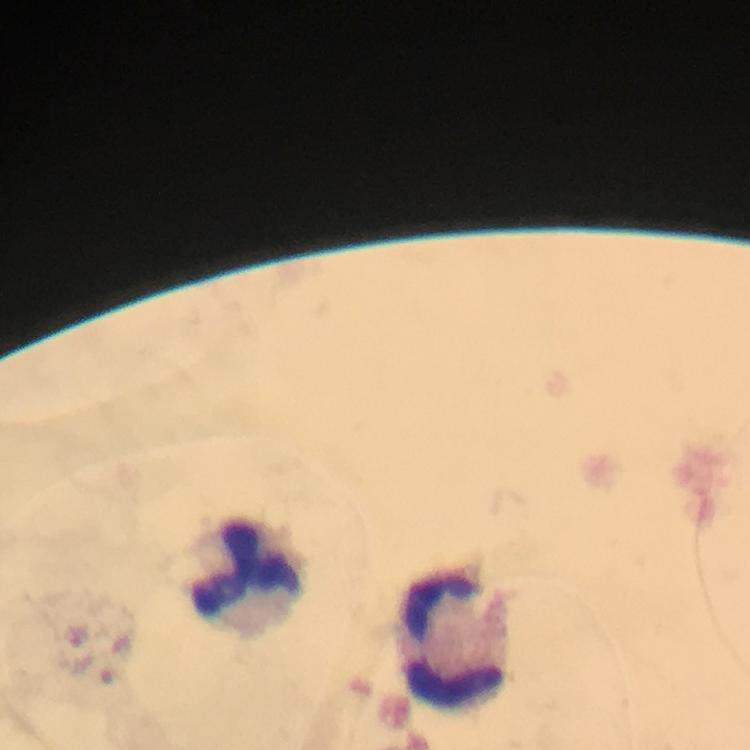
Approximate centers as (x, y) in pixels. Leukocyte locations: (248, 572), (456, 638). Image is 750×750 pixels. Giemsa-stained preparation. Immersion oil was used. Malaria parasites: none seen. Photographed with a smartphone mounted on the microscope. Cropped region of a single field of view. Thick blood film. From a malaria diagnostic workup. At 100x magnification.